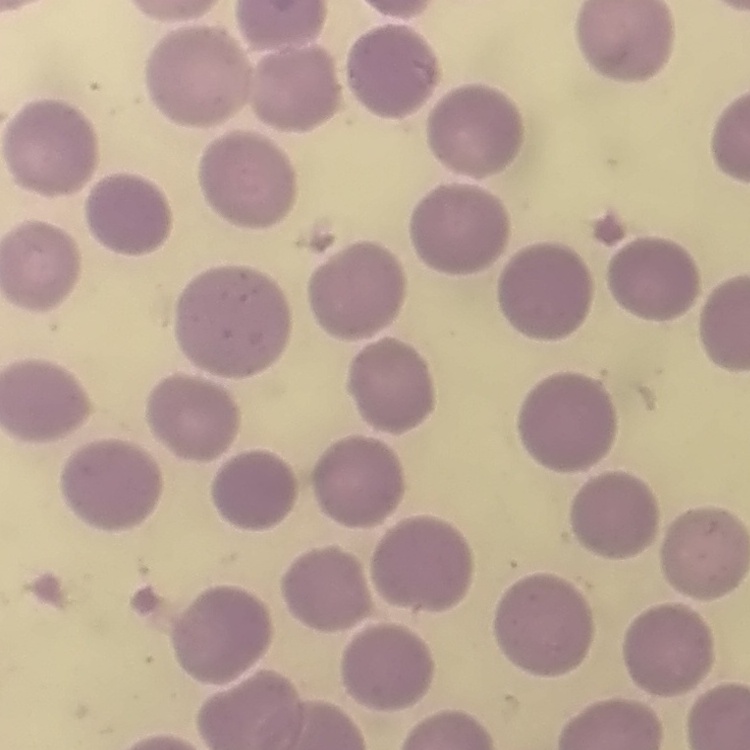

Summary:
  - Erythrocyte morphology: no rouleaux formation
  - Preparation: thin peripheral smear
  - Image type: square crop of a larger photomicrograph
  - Stain: Field's or Giemsa